Locate every Plasmodium parasite.
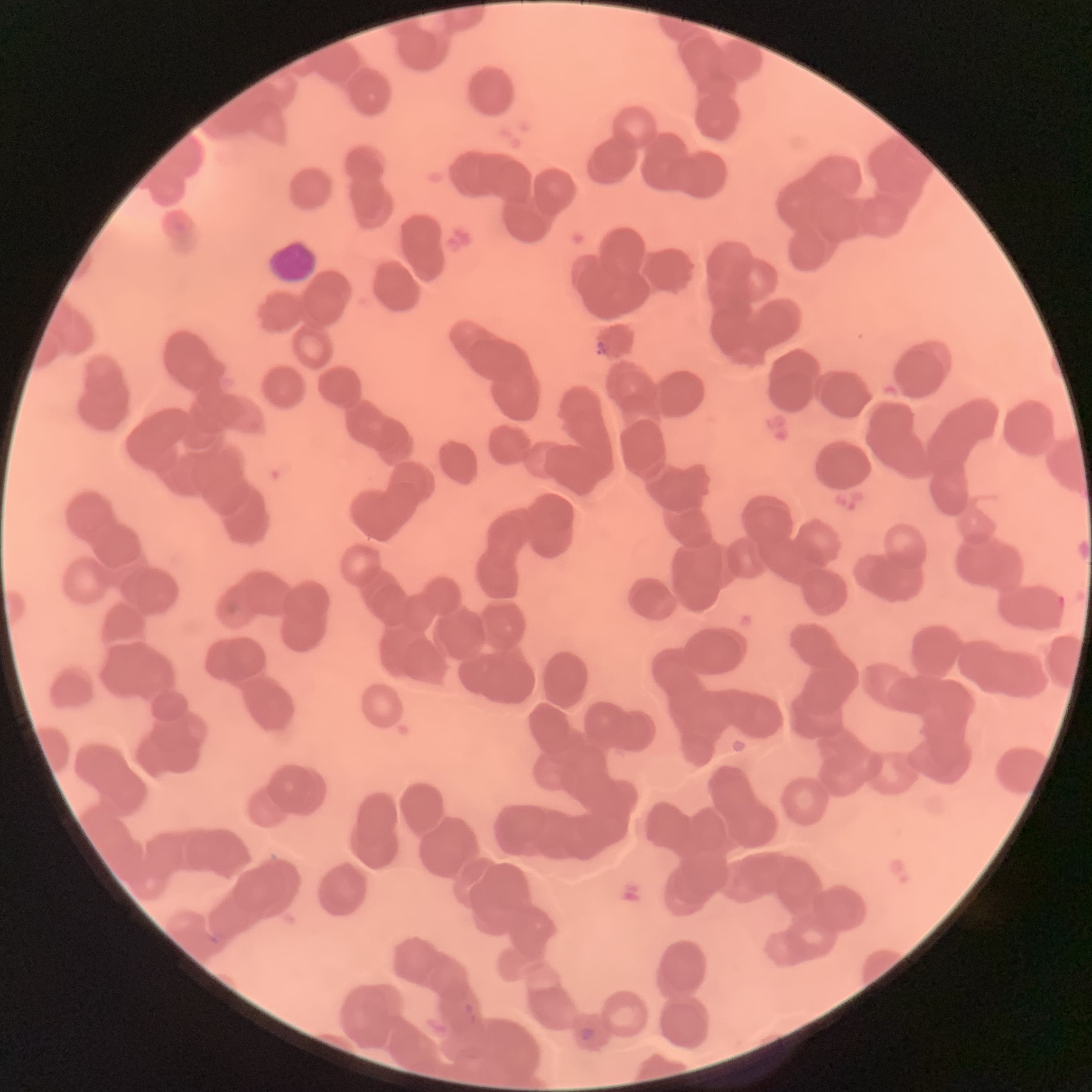
Approximate bounding boxes as (x1,y1)-(x2,y2) corner pairs in pixels.
Plasmodium parasites: (1056,594)-(1064,615), (226,598)-(244,616), (204,930)-(226,946), (461,1001)-(478,1024), (579,1026)-(596,1042).

Light microscopy. The red blood cells show rouleaux formation. Thin blood film. Image is 1092×1092 pixels.